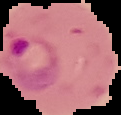
preparation = thin blood smear
malaria status = parasitized
image size = 121×115 pixels
image type = segmented cell region on a black background